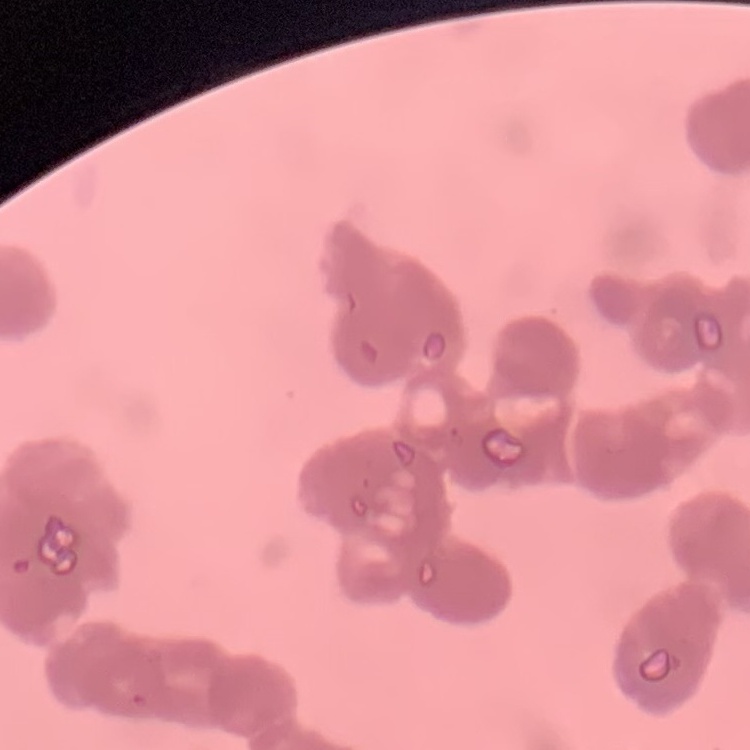
Summary:
  - Erythrocyte morphology: rouleaux formation
  - Image type: one tile cut from a larger photomicrograph
  - Preparation: thin peripheral smear
  - Stain: Field's or Giemsa